Report the malaria status of this cell.
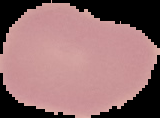

It is uninfected.

Image is 160×118 pixels. From a thin blood smear. Cell region segmented out of the field of view; the surrounding area is masked to black.